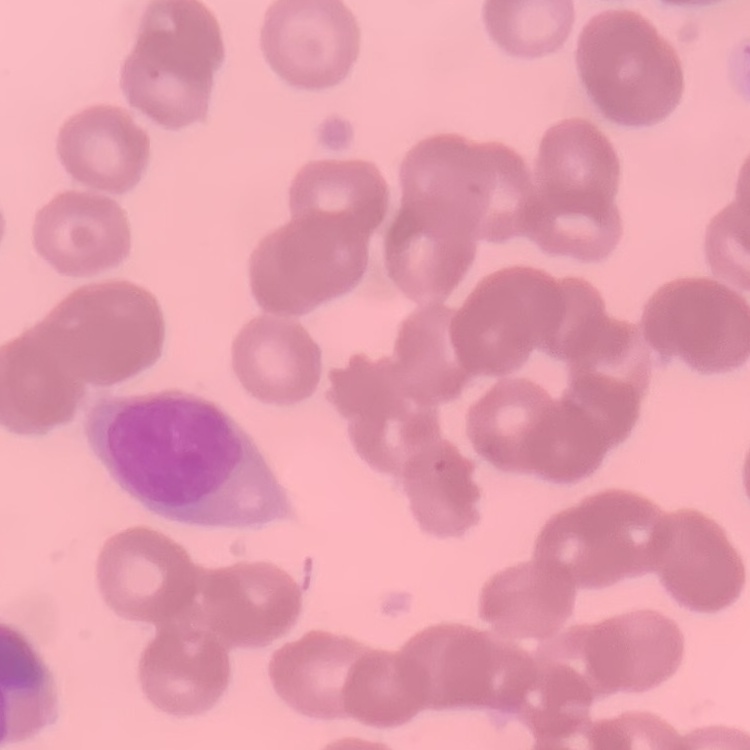

The red blood cells exhibit rouleaux formation. Thin blood smear. Square crop of a larger photomicrograph. Field's or Giemsa stain.